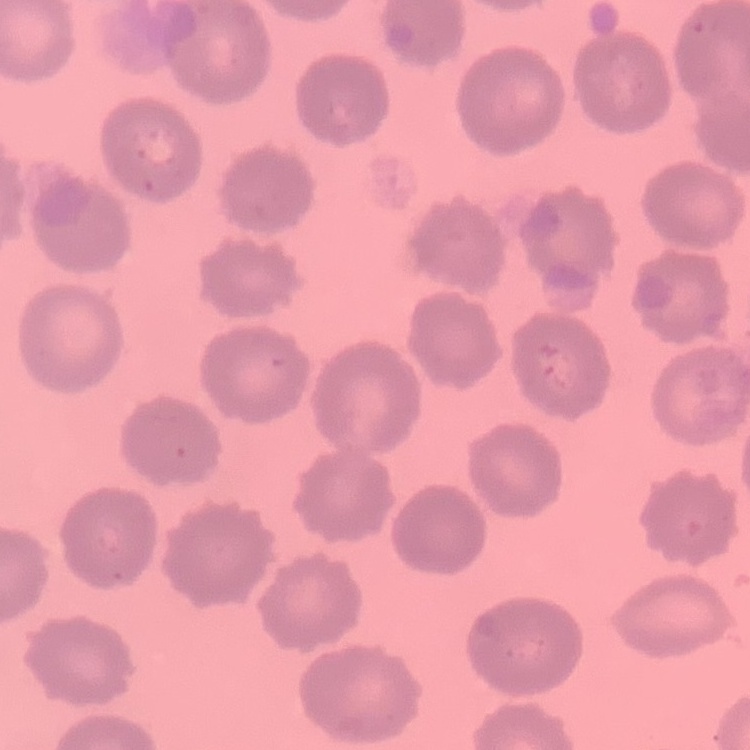
The erythrocytes exhibit no rouleaux formation. Square crop of a larger photomicrograph. Field's or Giemsa stain. Thin blood smear.